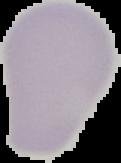
preparation = thin blood smear
image type = segmented cell region on a black background
image size = 121×163 pixels
result = negative for malaria parasites